Mark where platelets are.
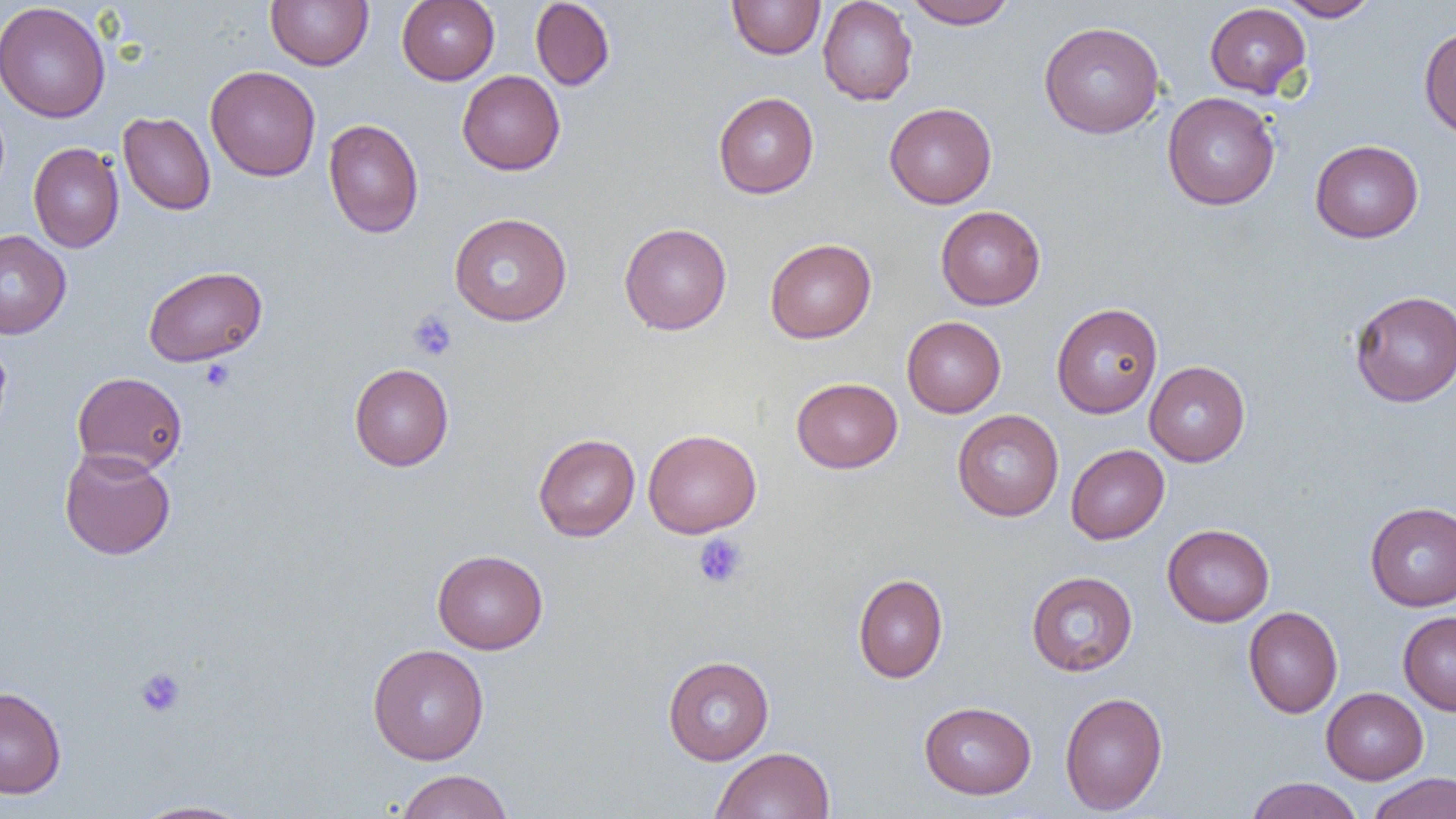

Approximate bounding boxes as [x1, y1, x2, y2] in pixels.
Platelets: [408, 310, 458, 361], [200, 358, 235, 393], [693, 534, 748, 589], [135, 666, 186, 718].

slide-level diagnosis = no evidence of blood parasites
image size = 1456×819 pixels
preparation = thin blood film
uninfected red blood cell locations = approximate bounding boxes as [x1, y1, x2, y2] in pixels: [265, 0, 373, 70], [396, 0, 499, 85], [530, 0, 615, 91], [727, 0, 825, 59], [818, 0, 918, 106], [906, 0, 1017, 29], [1278, 0, 1379, 21], [0, 2, 111, 123], [1204, 3, 1311, 98], [1038, 21, 1165, 139], [1419, 26, 1456, 138], [205, 65, 321, 181], [457, 70, 565, 175], [713, 92, 819, 198], [1162, 92, 1280, 210], [884, 102, 997, 209], [118, 111, 216, 216], [323, 118, 424, 237], [1310, 139, 1424, 243], [28, 142, 124, 253], [935, 205, 1046, 310], [449, 212, 572, 326], [619, 222, 732, 335], [0, 230, 71, 339], [765, 238, 876, 344], [142, 266, 268, 366], [1350, 290, 1456, 407], [1051, 302, 1163, 419], [901, 316, 1006, 418], [0, 335, 12, 440], [1144, 361, 1250, 467], [349, 363, 454, 471], [72, 371, 187, 475], [791, 377, 903, 473], [952, 409, 1064, 521], [643, 428, 761, 538], [533, 433, 640, 542], [1066, 444, 1169, 544], [59, 448, 176, 560], [1365, 501, 1456, 611], [1162, 523, 1275, 626], [432, 549, 548, 654], [1026, 570, 1138, 676], [852, 573, 948, 683], [1243, 606, 1343, 718], [1398, 612, 1456, 715], [367, 643, 489, 764], [663, 656, 774, 765], [0, 686, 67, 799], [1321, 687, 1429, 784], [1060, 691, 1168, 815], [919, 701, 1036, 799], [711, 746, 835, 819], [395, 769, 513, 819], [1366, 772, 1456, 819], [1244, 777, 1364, 819], [131, 800, 252, 819]
field of view = one of a larger specimen
magnification = 1000x
modality = light microscopy